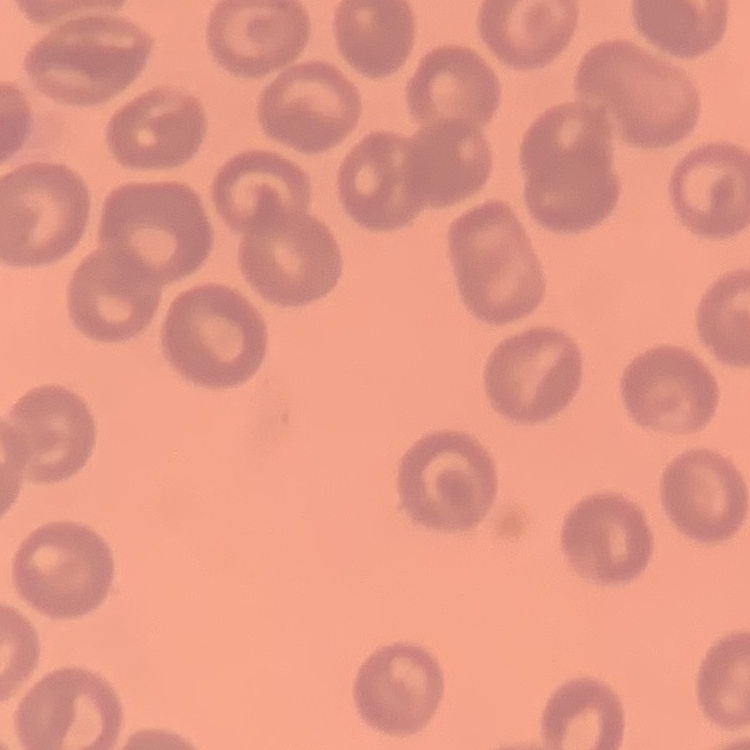
Summary:
  - Erythrocyte morphology: no rouleaux formation
  - Preparation: thin peripheral smear
  - Stain: Field's or Giemsa
  - Image type: one tile cut from a larger photomicrograph